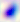

Captured at 400x magnification. Toxoplasma gondii is shown. Micrograph.